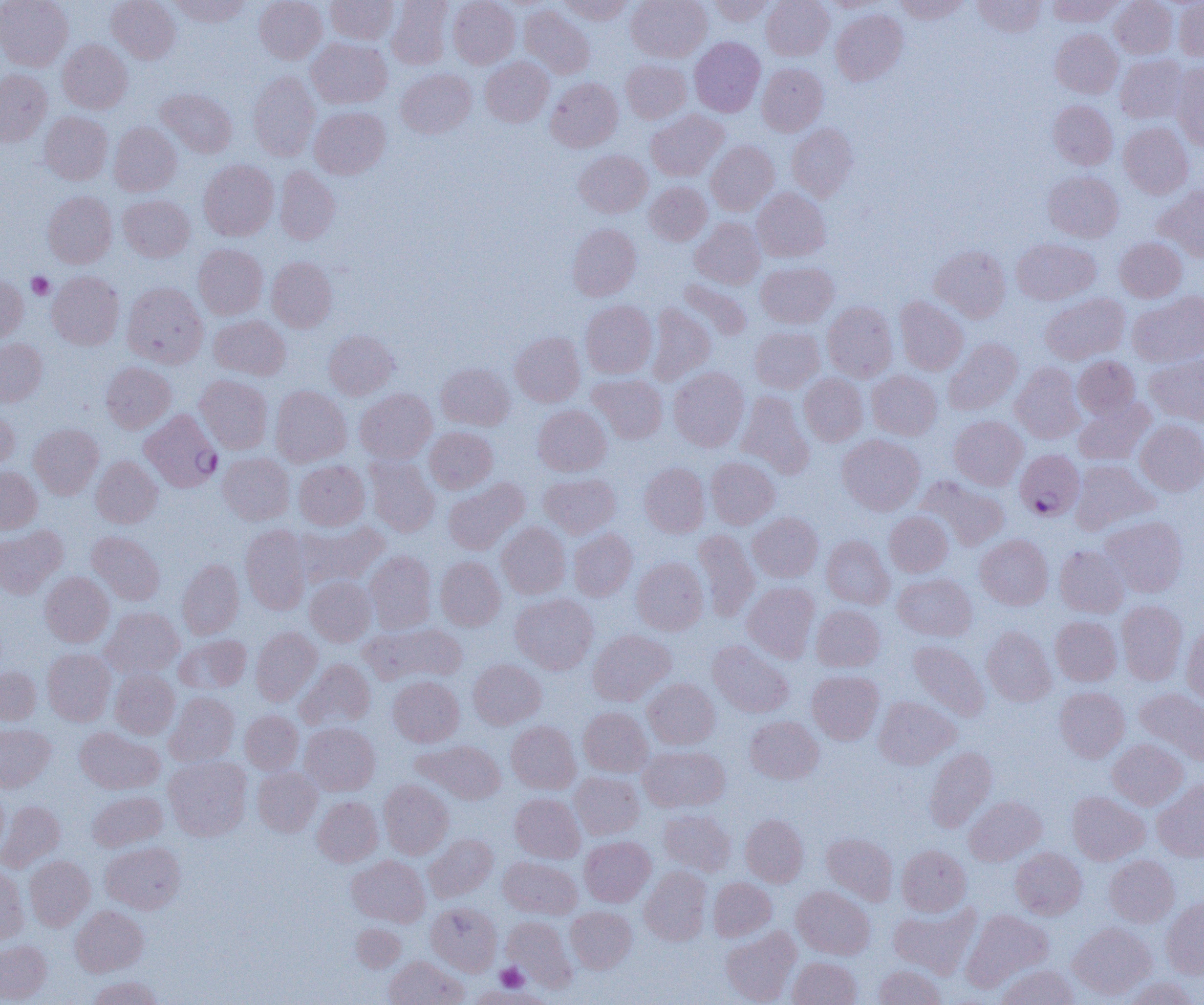

slide_level_diagnosis: Plasmodium falciparum
magnification: 1000x
field_of_view: single
modality: light microscopy
platelet_locations: 'approximate bounding boxes as (x1,y1)-(x2,y2) corner pairs in pixels: (26,272)-(54,300), (494,964)-(528,992)'
uninfected_red_blood_cell_locations: 'approximate bounding boxes as (x1,y1)-(x2,y2) corner pairs in pixels: (0,0)-(73,70), (106,0)-(180,64), (169,0)-(251,27), (254,0)-(327,63), (325,0)-(398,44), (448,0)-(520,68), (558,0)-(632,25), (626,0)-(711,62), (709,0)-(775,25), (762,0)-(833,60), (821,0)-(886,12), (894,0)-(970,23), (972,0)-(1045,37), (1110,0)-(1177,58), (386,1)-(453,69), (1047,1)-(1121,26), (1174,1)-(1204,61), (519,5)-(595,79), (831,9)-(907,85), (1051,29)-(1122,98), (690,37)-(765,116), (307,38)-(392,108), (58,39)-(132,113), (1115,54)-(1189,123), (481,57)-(553,126), (620,59)-(691,123), (757,63)-(828,136), (1171,63)-(1204,150), (396,68)-(476,138), (0,69)-(52,147), (248,71)-(320,160), (545,77)-(623,152), (156,88)-(237,158), (1048,100)-(1117,169), (310,106)-(390,179), (646,110)-(727,181), (39,111)-(112,184), (109,122)-(181,196), (1119,122)-(1193,198), (787,123)-(858,201), (706,141)-(779,215), (574,150)-(652,217), (199,159)-(279,241), (275,166)-(340,245), (1043,171)-(1123,242), (644,182)-(712,246), (1155,186)-(1204,262), (752,188)-(830,262), (42,191)-(117,268), (118,194)-(194,262), (691,218)-(765,289), (567,224)-(641,300), (1115,237)-(1187,301), (1011,238)-(1100,305), (193,244)-(268,319), (929,245)-(1010,322), (267,257)-(337,332), (756,262)-(838,328), (47,271)-(124,349), (0,275)-(28,343), (678,279)-(752,342), (122,282)-(208,367), (1128,291)-(1204,366), (1040,293)-(1129,364), (895,296)-(968,375), (581,300)-(657,378), (822,301)-(897,382), (646,303)-(716,385), (209,315)-(289,380), (750,327)-(825,393), (324,330)-(399,400), (510,332)-(585,406), (0,338)-(48,406), (943,338)-(1022,415), (1145,354)-(1204,426), (1073,356)-(1140,420), (101,362)-(175,433), (436,363)-(515,430), (1010,363)-(1085,443), (669,367)-(749,451), (867,370)-(942,440), (588,374)-(668,443), (799,374)-(868,446), (195,375)-(272,453), (270,385)-(351,466), (355,389)-(437,464), (736,391)-(814,477), (1074,399)-(1154,465), (533,405)-(611,476), (0,409)-(19,472), (949,415)-(1028,490), (1135,419)-(1204,496), (29,423)-(104,499), (425,427)-(498,493), (838,434)-(924,514), (218,452)-(294,525), (91,456)-(162,528), (365,456)-(439,536), (706,457)-(779,528), (1072,459)-(1158,534), (294,460)-(369,530), (639,462)-(709,537), (0,467)-(42,533), (539,473)-(621,538), (917,476)-(1009,551), (442,479)-(528,554), (884,511)-(952,577), (748,512)-(823,582), (1101,516)-(1188,597), (296,520)-(387,588), (497,522)-(570,598), (0,525)-(67,598), (240,525)-(310,614), (568,528)-(636,600), (693,528)-(759,621), (87,531)-(164,605), (975,534)-(1053,609), (822,535)-(894,608), (1055,545)-(1129,617), (364,550)-(436,633), (435,556)-(505,630), (632,557)-(708,635), (177,559)-(244,638), (40,571)-(114,647), (893,573)-(977,641), (305,577)-(376,646), (743,582)-(820,662), (510,593)-(598,674), (1116,600)-(1187,684), (811,604)-(885,671), (101,607)-(184,678), (1051,616)-(1121,685), (361,622)-(467,686), (1182,624)-(1204,707), (981,626)-(1056,706), (250,627)-(321,705), (587,629)-(676,706), (174,635)-(250,694), (908,640)-(990,721), (708,641)-(794,717), (42,648)-(115,726), (296,658)-(375,730), (468,659)-(546,729), (0,666)-(41,725), (110,669)-(179,738), (807,670)-(883,744), (388,676)-(464,747), (643,678)-(720,749), (1055,686)-(1129,762), (1135,687)-(1204,766), (165,691)-(239,766), (874,696)-(959,769), (578,707)-(652,777), (240,710)-(303,774), (745,716)-(823,784), (506,721)-(580,793), (300,722)-(380,795), (0,723)-(55,791), (75,727)-(164,793), (1108,738)-(1188,810), (413,740)-(506,804), (639,744)-(730,812), (924,746)-(997,831), (164,757)-(251,841), (252,767)-(322,836), (570,772)-(644,839), (379,779)-(454,858), (1153,781)-(1204,861), (0,785)-(8,856), (88,790)-(167,851), (1067,791)-(1150,864), (510,793)-(584,862), (313,796)-(382,866), (964,796)-(1046,865), (0,801)-(65,871), (659,809)-(736,875), (741,814)-(808,886), (821,832)-(898,905), (424,835)-(497,902), (579,836)-(655,907), (101,841)-(185,913), (897,844)-(971,916), (1010,847)-(1087,919), (25,855)-(95,930), (347,855)-(429,927), (1105,855)-(1179,927), (499,857)-(582,918), (0,865)-(28,945), (640,867)-(711,945), (708,877)-(776,941), (792,886)-(874,960), (1161,897)-(1204,979), (426,902)-(501,976), (889,904)-(980,978), (71,905)-(148,976), (566,906)-(636,973), (962,909)-(1052,991), (501,916)-(576,990), (1068,922)-(1156,1000), (351,923)-(406,971), (720,926)-(800,1005), (0,940)-(51,1003), (383,956)-(468,1005), (788,956)-(861,1005), (996,964)-(1078,1005), (873,965)-(946,1005), (88,976)-(162,1005), (1122,977)-(1200,1005), (467,985)-(549,1005)'
image_size: 1204×1005 pixels
plasmodium_falciparum_infected_red_blood_cell_locations: 'approximate bounding boxes as (x1,y1)-(x2,y2) corner pairs in pixels: (139,409)-(222,492), (1015,450)-(1084,520)'
preparation: thin blood smear